State which parasite is depicted.
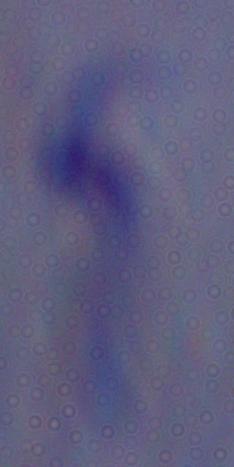

This is a trypanosome.

Summary:
  - Magnification: 1000x
  - Modality: micrograph